Locate every leukocyte (white blood cell).
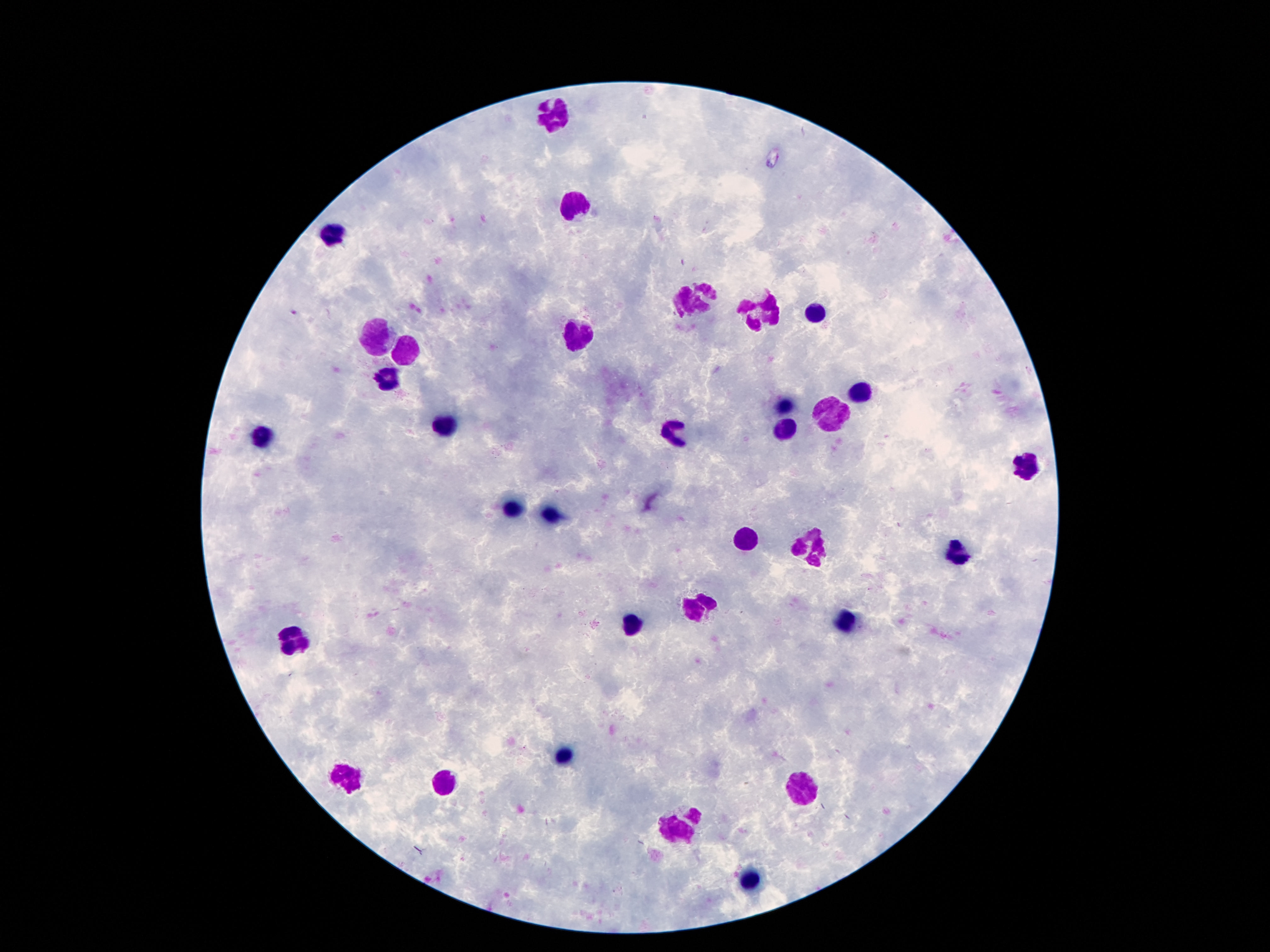
Approximate object centers, in pixels from the top-left corner.
Leukocytes: (x=557, y=113), (x=578, y=204), (x=333, y=234), (x=695, y=302), (x=816, y=314), (x=760, y=317), (x=578, y=333), (x=377, y=334), (x=405, y=349), (x=384, y=379), (x=861, y=394), (x=788, y=407), (x=835, y=412), (x=443, y=425), (x=783, y=428), (x=676, y=431), (x=263, y=433), (x=1022, y=463), (x=510, y=505), (x=550, y=514), (x=748, y=540), (x=814, y=544), (x=959, y=552), (x=690, y=606), (x=636, y=621), (x=849, y=626), (x=291, y=640), (x=566, y=753), (x=347, y=778), (x=443, y=785), (x=802, y=785), (x=681, y=827), (x=751, y=879).

image size = 1270×952 pixels
magnification = 100x
preparation = thick blood smear
field of view = single
capture = smartphone camera through the microscope eyepiece
stain = Giemsa
patient malaria status = uninfected